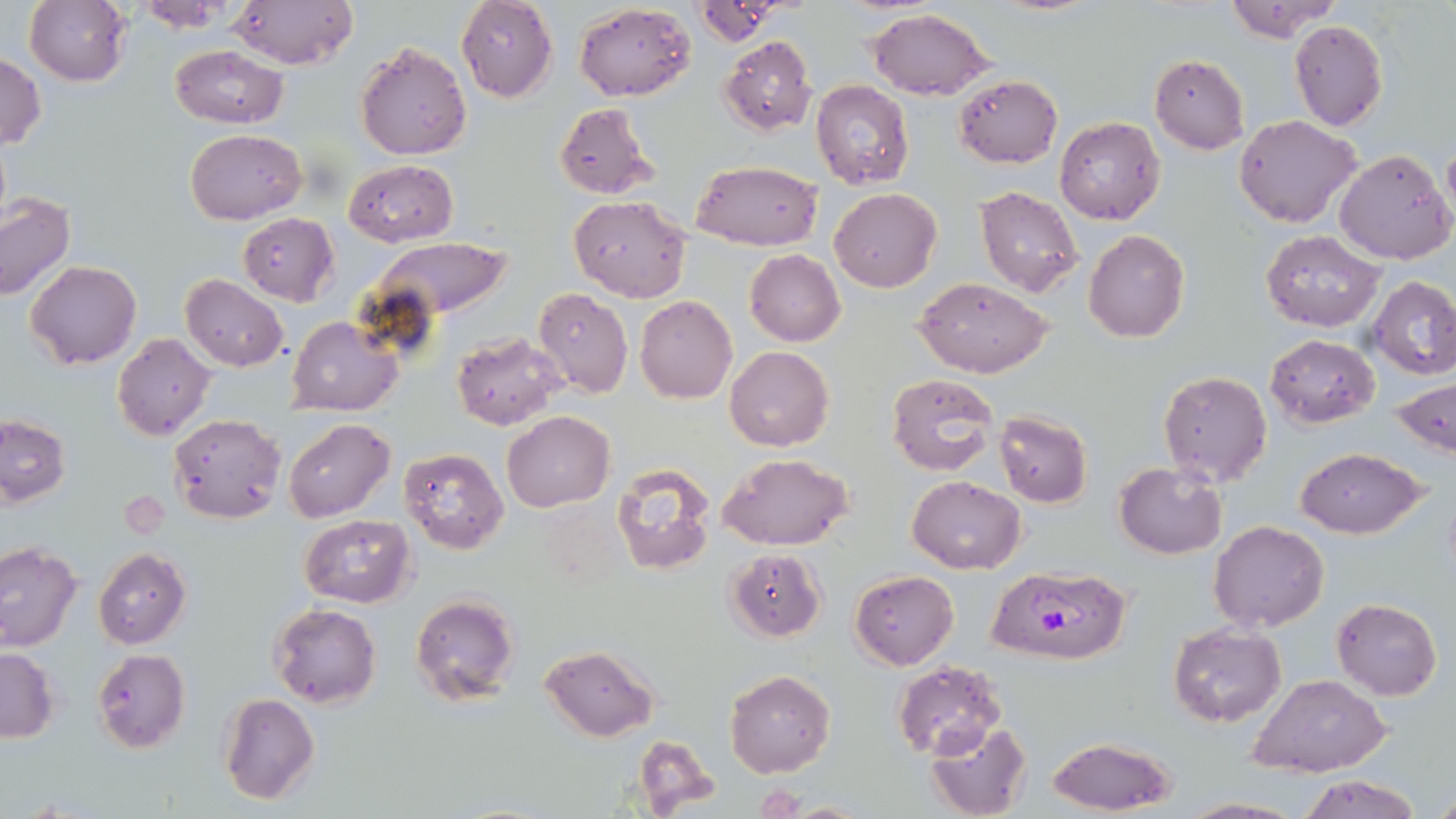
Approximate bounding boxes as named x1/y1/x2/y2 corners in pixels. Plasmodium falciparum-infected red blood cell locations: (x1=992, y1=567, x2=1133, y2=665). Uninfected red blood cell locations: (x1=25, y1=0, x2=133, y2=87), (x1=131, y1=0, x2=243, y2=29), (x1=227, y1=0, x2=357, y2=70), (x1=456, y1=0, x2=558, y2=103), (x1=1224, y1=0, x2=1344, y2=43), (x1=575, y1=3, x2=695, y2=100), (x1=868, y1=8, x2=995, y2=101), (x1=1288, y1=20, x2=1388, y2=131), (x1=719, y1=35, x2=817, y2=135), (x1=354, y1=40, x2=472, y2=160), (x1=168, y1=45, x2=290, y2=129), (x1=0, y1=50, x2=44, y2=150), (x1=1149, y1=53, x2=1249, y2=154), (x1=954, y1=74, x2=1062, y2=167), (x1=810, y1=79, x2=916, y2=189), (x1=554, y1=102, x2=659, y2=200), (x1=1234, y1=114, x2=1362, y2=229), (x1=1054, y1=115, x2=1166, y2=225), (x1=186, y1=129, x2=307, y2=223), (x1=1334, y1=148, x2=1455, y2=264), (x1=343, y1=159, x2=458, y2=247), (x1=692, y1=161, x2=823, y2=250), (x1=975, y1=185, x2=1083, y2=297), (x1=829, y1=188, x2=942, y2=291), (x1=0, y1=193, x2=75, y2=301), (x1=568, y1=195, x2=693, y2=302), (x1=236, y1=213, x2=339, y2=307), (x1=1260, y1=229, x2=1385, y2=331), (x1=1084, y1=231, x2=1189, y2=342), (x1=364, y1=236, x2=516, y2=325), (x1=745, y1=249, x2=844, y2=346), (x1=25, y1=261, x2=142, y2=368), (x1=180, y1=274, x2=288, y2=372), (x1=1368, y1=274, x2=1456, y2=379), (x1=916, y1=277, x2=1055, y2=379), (x1=532, y1=286, x2=632, y2=398), (x1=635, y1=295, x2=738, y2=403), (x1=288, y1=316, x2=402, y2=417), (x1=452, y1=331, x2=566, y2=430), (x1=112, y1=333, x2=217, y2=441), (x1=1265, y1=333, x2=1379, y2=428), (x1=724, y1=345, x2=834, y2=452), (x1=1156, y1=370, x2=1272, y2=487), (x1=887, y1=372, x2=996, y2=476), (x1=1392, y1=376, x2=1456, y2=458), (x1=993, y1=410, x2=1092, y2=507), (x1=501, y1=411, x2=614, y2=511), (x1=168, y1=414, x2=286, y2=523), (x1=0, y1=415, x2=71, y2=508), (x1=283, y1=418, x2=394, y2=522), (x1=400, y1=447, x2=509, y2=554), (x1=1294, y1=447, x2=1428, y2=540), (x1=721, y1=454, x2=853, y2=551), (x1=1113, y1=462, x2=1227, y2=559), (x1=610, y1=463, x2=718, y2=576), (x1=908, y1=476, x2=1025, y2=573), (x1=300, y1=515, x2=415, y2=608), (x1=1209, y1=521, x2=1330, y2=632), (x1=0, y1=542, x2=81, y2=651), (x1=93, y1=547, x2=191, y2=649), (x1=726, y1=548, x2=827, y2=641), (x1=849, y1=570, x2=959, y2=669), (x1=411, y1=593, x2=521, y2=707), (x1=1330, y1=598, x2=1442, y2=701), (x1=269, y1=604, x2=381, y2=710), (x1=1168, y1=623, x2=1286, y2=727), (x1=540, y1=645, x2=659, y2=741), (x1=0, y1=648, x2=59, y2=741), (x1=91, y1=650, x2=189, y2=752), (x1=892, y1=659, x2=1008, y2=762), (x1=724, y1=670, x2=835, y2=777), (x1=1247, y1=674, x2=1390, y2=777), (x1=219, y1=693, x2=319, y2=805), (x1=924, y1=719, x2=1031, y2=819), (x1=631, y1=733, x2=723, y2=816), (x1=1046, y1=736, x2=1177, y2=816), (x1=1297, y1=774, x2=1422, y2=819), (x1=1431, y1=786, x2=1456, y2=815), (x1=1178, y1=798, x2=1305, y2=819). Slide-level diagnosis: Plasmodium falciparum. Captured at 1000x magnification. Optical microscopy. May-Grünwald-Giemsa stain. One field of a larger specimen. Thin blood smear. Image is 1456×819 pixels.